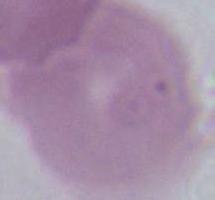

Summary:
  - Identification: erythrocyte
  - Magnification: 1000x
  - Modality: photomicrograph